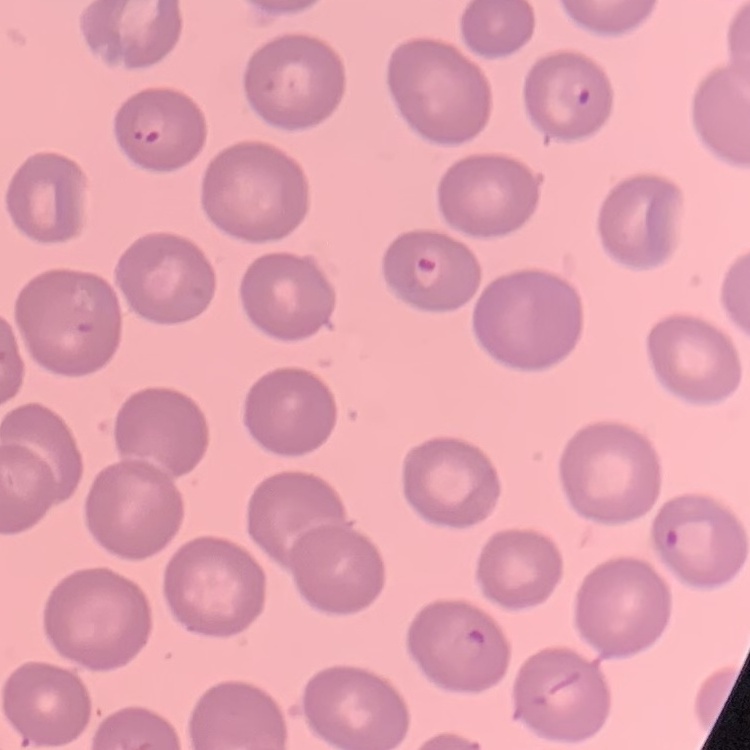

The erythrocytes show no rouleaux formation. Thin blood film. Field's or Giemsa stain. One tile cut from a larger photomicrograph.